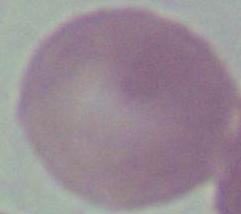

Summary:
  - Magnification: 1000x
  - Modality: photomicrograph
  - Identification: red blood cell